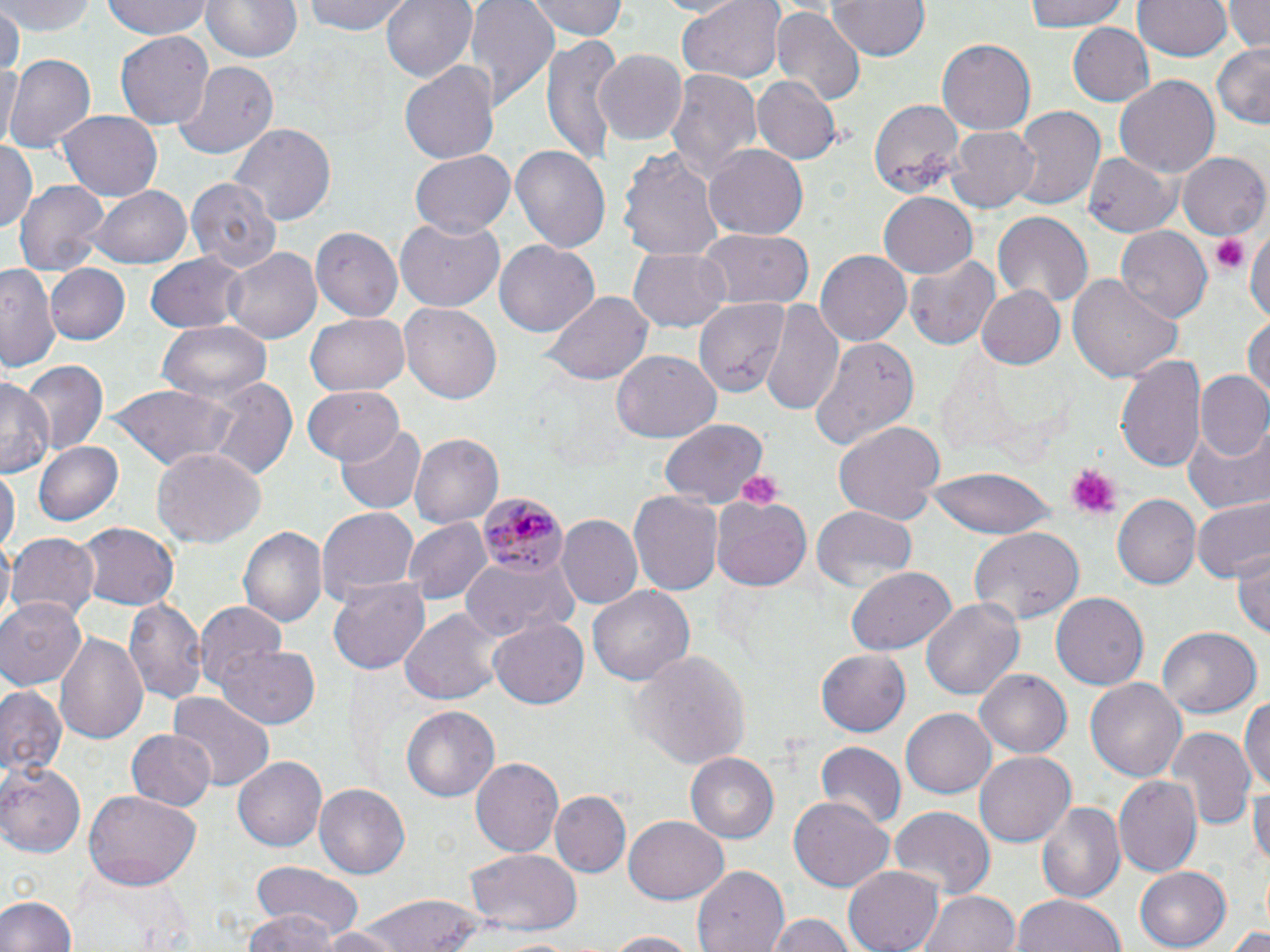

Summary:
  - Coordinate format: approximate bounding boxes as (x1, y1, x2, y2) in pixels
  - Plasmodium malariae-infected red blood cell locations: (480, 492, 565, 579)
  - Uninfected red blood cell locations: (6, 0, 97, 35), (101, 0, 216, 41), (201, 0, 299, 63), (302, 0, 411, 37), (381, 0, 477, 84), (464, 0, 560, 106), (528, 0, 629, 41), (657, 0, 741, 17), (828, 0, 930, 61), (1022, 0, 1132, 32), (1223, 0, 1270, 53), (675, 1, 787, 82), (1134, 1, 1231, 62), (771, 6, 865, 107), (0, 7, 22, 81), (4, 10, 46, 59), (1066, 22, 1156, 105), (116, 28, 214, 127), (542, 37, 622, 169), (938, 39, 1036, 135), (1211, 42, 1270, 129), (596, 48, 688, 144), (6, 54, 95, 156), (0, 58, 18, 155), (401, 61, 500, 164), (173, 63, 277, 160), (663, 67, 760, 184), (1114, 75, 1219, 179), (754, 76, 840, 163), (866, 95, 966, 196), (1010, 105, 1103, 211), (59, 110, 163, 201), (231, 123, 338, 225), (947, 126, 1040, 214), (0, 137, 36, 236), (704, 143, 808, 237), (510, 144, 611, 256), (617, 144, 724, 260), (1178, 149, 1270, 240), (1084, 150, 1180, 237), (410, 151, 515, 237), (187, 174, 281, 271), (13, 178, 110, 275), (90, 185, 192, 268), (878, 193, 977, 280), (993, 212, 1093, 307), (394, 220, 504, 312), (1247, 220, 1270, 330), (312, 225, 404, 320), (1115, 226, 1211, 324), (696, 229, 814, 310), (495, 240, 599, 337), (223, 246, 321, 345), (630, 248, 729, 331), (816, 250, 911, 347), (145, 253, 248, 334), (905, 254, 1003, 350), (43, 263, 130, 346), (0, 265, 61, 373), (1067, 274, 1184, 384), (975, 285, 1067, 370), (541, 290, 654, 387), (763, 297, 846, 418), (694, 298, 789, 398), (400, 302, 503, 405), (305, 313, 410, 397), (1244, 314, 1270, 408), (156, 320, 273, 404), (808, 337, 918, 452), (613, 351, 720, 442), (1117, 352, 1203, 474), (21, 360, 106, 456), (1197, 370, 1269, 460), (0, 375, 54, 479), (207, 376, 298, 480), (301, 385, 403, 465), (103, 386, 238, 470), (660, 420, 767, 505), (835, 420, 946, 526), (1186, 423, 1270, 513), (336, 427, 426, 515), (411, 433, 504, 529), (35, 440, 123, 527), (152, 446, 267, 548), (0, 467, 18, 558), (926, 468, 1058, 538), (629, 490, 722, 594), (711, 492, 814, 591), (1114, 496, 1200, 589), (1191, 497, 1269, 582), (316, 505, 420, 611), (810, 508, 918, 594), (555, 515, 642, 611), (406, 518, 490, 605), (74, 522, 179, 612), (238, 526, 327, 628), (971, 526, 1084, 624), (8, 535, 100, 627), (1232, 546, 1270, 641), (460, 558, 574, 636), (845, 566, 955, 655), (327, 576, 431, 675), (588, 584, 696, 683), (124, 594, 208, 704), (1052, 594, 1147, 689), (0, 596, 88, 688), (922, 596, 1024, 702), (195, 602, 287, 692), (400, 606, 504, 704), (488, 615, 590, 710), (1158, 626, 1263, 719), (53, 629, 150, 746), (217, 640, 321, 729), (627, 649, 751, 771), (817, 649, 912, 735), (974, 666, 1071, 755), (1085, 675, 1186, 779), (0, 683, 68, 782), (168, 692, 277, 789), (1241, 693, 1270, 794), (402, 705, 500, 800), (901, 709, 995, 798), (1165, 725, 1255, 832), (125, 729, 216, 811), (814, 742, 907, 830), (975, 751, 1075, 846), (686, 752, 779, 845), (233, 756, 325, 853), (471, 757, 562, 858), (0, 765, 81, 857), (1249, 774, 1270, 875), (1114, 776, 1203, 878), (315, 782, 411, 879), (553, 790, 630, 876), (85, 791, 200, 886), (789, 797, 894, 893), (1037, 798, 1128, 904), (888, 806, 996, 898), (625, 817, 728, 905), (465, 850, 582, 933), (844, 864, 944, 952), (76, 865, 194, 951), (249, 866, 361, 938), (693, 866, 786, 951), (1135, 867, 1231, 949), (918, 889, 1021, 952), (0, 892, 78, 952), (352, 893, 490, 952), (1011, 893, 1124, 952), (246, 910, 339, 952), (766, 914, 862, 952), (304, 926, 414, 951), (1228, 926, 1270, 952), (603, 930, 698, 951), (491, 936, 586, 952)
  - Platelet locations: (1208, 231, 1249, 277), (1065, 465, 1119, 518), (732, 468, 784, 508)
  - Slide-level diagnosis: Plasmodium malariae
  - Image size: 1270×952 pixels
  - Stain: May-Grünwald-Giemsa
  - Magnification: 1000x
  - Modality: light microscopy
  - Preparation: thin blood smear
  - Field of view: single